Outline each uninfected red blood cell.
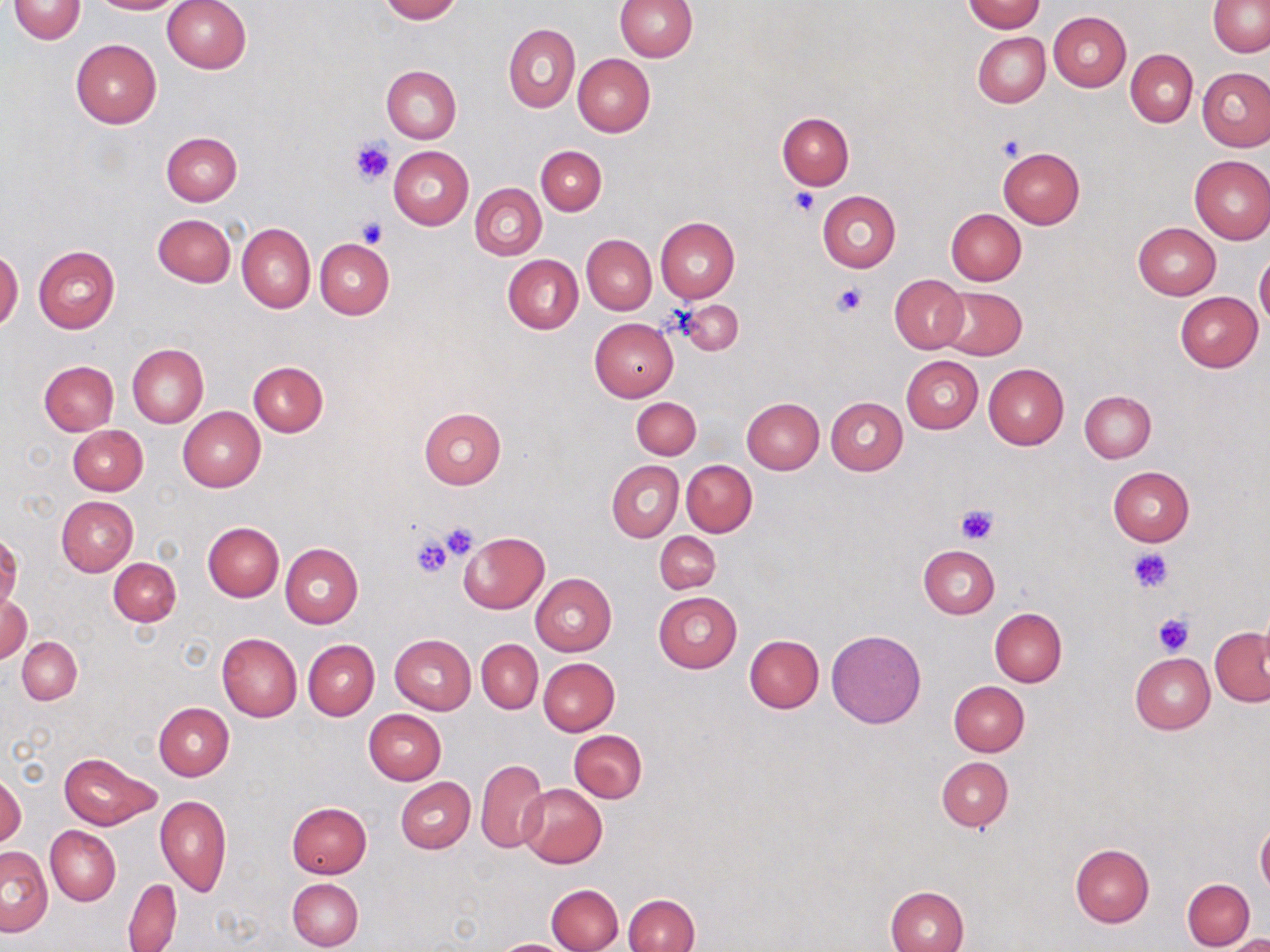

Approximate bounding boxes as (x1, y1, x2, y2) in pixels.
Uninfected red blood cells: (9, 0, 85, 43), (89, 0, 181, 14), (162, 0, 252, 74), (378, 0, 460, 22), (614, 0, 697, 62), (1208, 0, 1270, 56), (960, 1, 1045, 33), (1049, 11, 1131, 91), (503, 23, 579, 112), (973, 32, 1050, 107), (70, 38, 161, 128), (1125, 50, 1198, 127), (573, 53, 655, 137), (382, 65, 462, 143), (1198, 67, 1270, 151), (776, 112, 854, 189), (162, 132, 242, 206), (388, 146, 473, 229), (536, 146, 606, 214), (998, 147, 1085, 228), (1189, 155, 1270, 244), (470, 182, 546, 259), (817, 190, 901, 272), (946, 209, 1026, 285), (152, 213, 235, 287), (654, 217, 739, 303), (1133, 222, 1221, 300), (237, 223, 315, 313), (582, 235, 655, 314), (314, 238, 394, 318), (33, 245, 120, 333), (0, 249, 23, 330), (1255, 250, 1270, 329), (503, 254, 583, 334), (890, 274, 968, 353), (936, 287, 1027, 359), (1175, 292, 1263, 372), (590, 318, 679, 402), (128, 343, 209, 427), (902, 355, 983, 434), (40, 361, 118, 435), (249, 361, 327, 437), (983, 363, 1069, 449), (1079, 389, 1156, 463), (631, 397, 701, 458), (741, 398, 824, 474), (826, 398, 907, 475), (178, 406, 265, 491), (419, 407, 506, 488), (68, 424, 147, 495), (606, 460, 684, 542), (682, 461, 756, 536), (1108, 465, 1195, 545), (57, 496, 139, 576), (202, 522, 283, 601), (458, 531, 549, 614), (655, 532, 720, 593), (280, 542, 363, 627), (918, 544, 1000, 619), (109, 558, 181, 625), (531, 574, 616, 656), (0, 591, 31, 664), (653, 591, 742, 673), (1256, 604, 1270, 677), (989, 608, 1066, 686), (1210, 628, 1270, 705), (827, 629, 926, 728), (217, 632, 302, 721), (390, 634, 476, 714), (743, 634, 824, 713), (18, 637, 82, 705), (303, 639, 379, 720), (477, 640, 542, 713), (1130, 654, 1214, 733), (538, 657, 619, 735), (949, 681, 1029, 756), (154, 702, 234, 780), (362, 709, 446, 785), (569, 730, 647, 803), (60, 752, 159, 829), (936, 757, 1012, 831), (476, 758, 546, 853), (1, 771, 25, 849), (396, 778, 474, 853), (517, 784, 607, 868), (156, 795, 231, 895), (287, 801, 372, 878), (1256, 821, 1270, 896), (46, 826, 120, 904), (1071, 844, 1154, 927), (1, 847, 52, 936), (124, 878, 182, 952), (287, 878, 363, 951), (1182, 878, 1254, 950), (547, 883, 623, 952), (885, 886, 968, 952), (624, 894, 699, 952), (1220, 933, 1270, 951), (492, 938, 575, 951).

Summary:
  - Platelet locations: (997, 133, 1028, 161), (351, 138, 394, 187), (790, 188, 821, 217), (358, 218, 387, 247), (834, 283, 866, 315), (956, 505, 1000, 546), (438, 522, 482, 562), (409, 533, 455, 579), (1130, 548, 1171, 592), (1153, 612, 1193, 654)
  - Slide-level diagnosis: negative for blood parasites
  - Image size: 1270×952 pixels
  - Modality: light microscopy
  - Preparation: thin blood film
  - Stain: May-Grünwald-Giemsa
  - Field of view: single
  - Magnification: 1000x